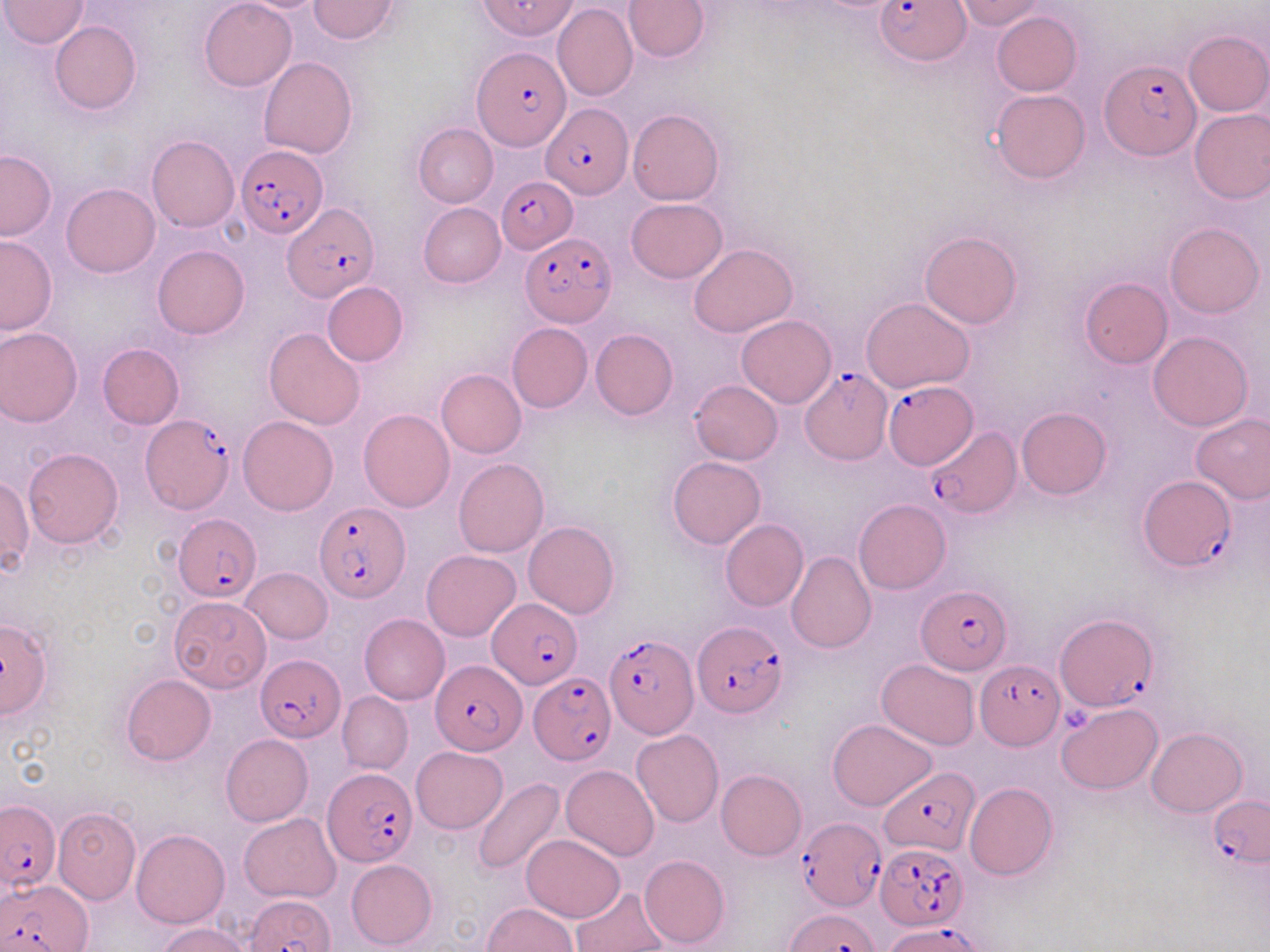

Approximate bounding boxes as [x1, y1, x2, y2] in pixels. Plasmodium falciparum-infected red blood cell locations: [481, 0, 577, 41], [876, 0, 970, 66], [474, 46, 569, 150], [1099, 58, 1199, 160], [541, 103, 632, 198], [237, 146, 327, 237], [495, 176, 577, 253], [281, 203, 379, 303], [522, 232, 616, 325], [800, 368, 890, 464], [884, 380, 977, 468], [139, 414, 235, 515], [927, 426, 1017, 516], [1139, 476, 1234, 572], [315, 502, 409, 601], [174, 514, 262, 599], [917, 586, 1012, 673], [487, 600, 583, 688], [1054, 613, 1155, 712], [691, 622, 787, 718], [605, 634, 697, 739], [255, 654, 345, 742], [429, 659, 528, 754], [975, 660, 1066, 751], [527, 671, 616, 765], [879, 767, 981, 856], [323, 768, 418, 867], [1209, 795, 1270, 867], [0, 799, 60, 892], [796, 817, 885, 913], [875, 840, 968, 929], [4, 877, 93, 952], [243, 894, 337, 951], [786, 908, 880, 952], [886, 921, 985, 952]. Uninfected red blood cell locations: [2, 0, 90, 48], [199, 0, 297, 91], [308, 0, 400, 42], [624, 0, 711, 61], [956, 1, 1046, 29], [552, 4, 638, 102], [991, 11, 1081, 96], [50, 20, 142, 115], [1183, 30, 1270, 117], [258, 56, 358, 158], [991, 89, 1089, 183], [627, 108, 724, 205], [1189, 108, 1270, 203], [413, 123, 498, 207], [147, 136, 239, 233], [0, 150, 56, 240], [61, 183, 159, 277], [626, 198, 727, 283], [418, 203, 506, 288], [1165, 222, 1264, 318], [920, 232, 1022, 329], [0, 234, 58, 334], [689, 243, 797, 337], [153, 244, 249, 338], [1079, 276, 1173, 368], [322, 281, 408, 366], [861, 297, 974, 393], [736, 314, 836, 408], [507, 323, 592, 412], [1, 327, 81, 427], [263, 328, 366, 430], [590, 329, 678, 420], [1148, 331, 1254, 431], [98, 344, 184, 429], [436, 368, 526, 458], [689, 380, 782, 465], [1017, 407, 1111, 500], [358, 409, 455, 513], [1190, 412, 1270, 503], [239, 416, 338, 515], [22, 447, 124, 548], [667, 456, 766, 549], [453, 458, 549, 558], [1, 475, 33, 577], [853, 498, 950, 594], [720, 519, 809, 612], [523, 521, 619, 618], [421, 550, 520, 641], [786, 552, 876, 654], [241, 567, 332, 644], [167, 596, 272, 693], [359, 614, 449, 704], [0, 616, 55, 719], [877, 658, 980, 750], [122, 674, 216, 765], [337, 692, 413, 774], [1056, 703, 1161, 794], [828, 719, 938, 811], [1147, 728, 1247, 817], [631, 729, 723, 828], [220, 734, 313, 827], [411, 746, 508, 834], [561, 764, 659, 862], [716, 769, 807, 860], [470, 779, 565, 877], [964, 782, 1058, 879], [53, 806, 141, 904], [240, 812, 343, 902], [45, 816, 220, 911], [132, 829, 230, 928], [522, 834, 626, 922], [640, 854, 730, 948], [346, 858, 437, 948], [571, 888, 668, 952], [483, 902, 577, 951], [156, 923, 253, 952]. Platelet locations: [1062, 708, 1092, 733]. Slide-level diagnosis: Plasmodium falciparum. Image is 1270×952 pixels. Single field of view. May-Grünwald-Giemsa-stained preparation. 1000x magnification. Thin blood smear. Optical microscopy.